Give the position of every Plasmodium parasite.
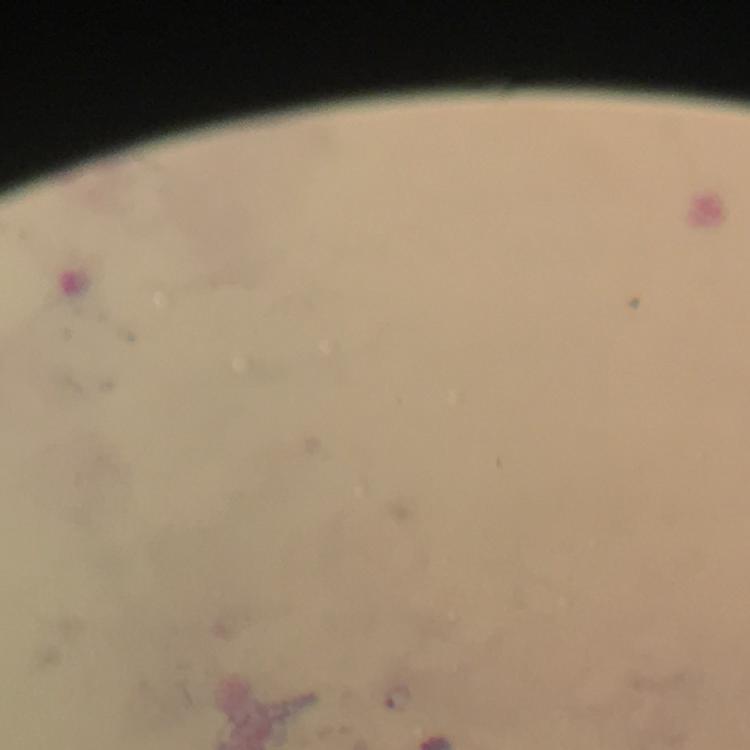

Approximate centers as {x, y} in pixels.
Plasmodium parasites: {400, 698}.

Thick smear. At 100x magnification. Photographed with a smartphone mounted on the microscope. From a diagnostic examination for malaria. A crop from one field of view. Giemsa-stained preparation. Immersion oil applied. Image is 750×750 pixels.